Report the malaria status of this cell.
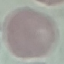

It is uninfected.

Summary:
  - Capture: smartphone camera at the microscope eyepiece
  - Stain: Giemsa
  - Preparation: thin blood smear
  - Image type: cell patch, automatically extracted from a larger field of view and resized to 64 × 64 pixels